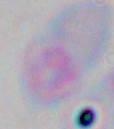

identification: Toxoplasma gondii
modality: micrograph
magnification: 1000x